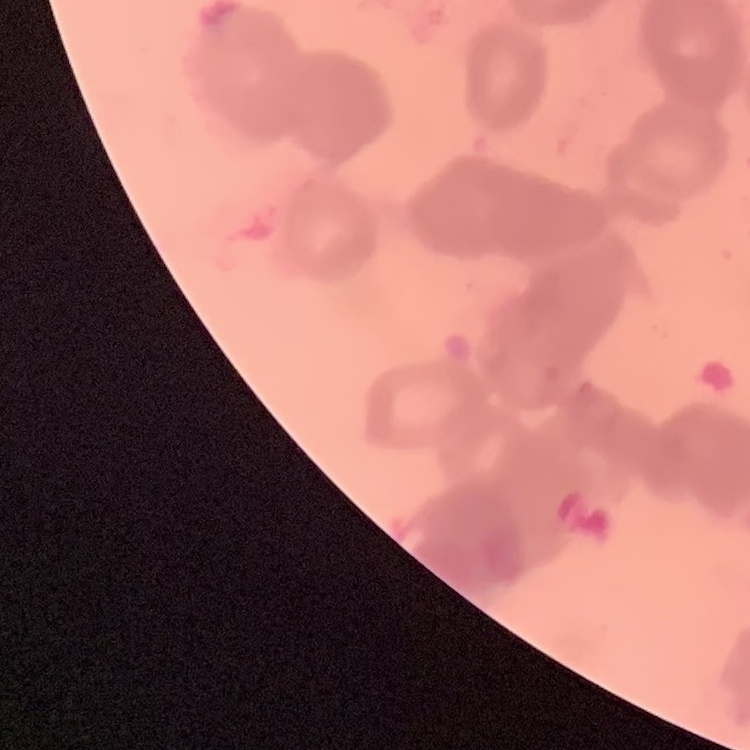

Summary:
  - Red blood cell morphology: rouleaux formation
  - Preparation: thin peripheral smear
  - Image type: square crop of a larger photomicrograph
  - Stain: Field's or Giemsa